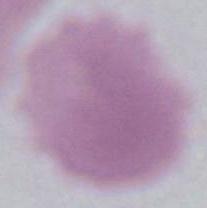
Summary:
  - Modality: photomicrograph
  - Identification: erythrocyte
  - Magnification: 1000x